Identify the blood parasite species.
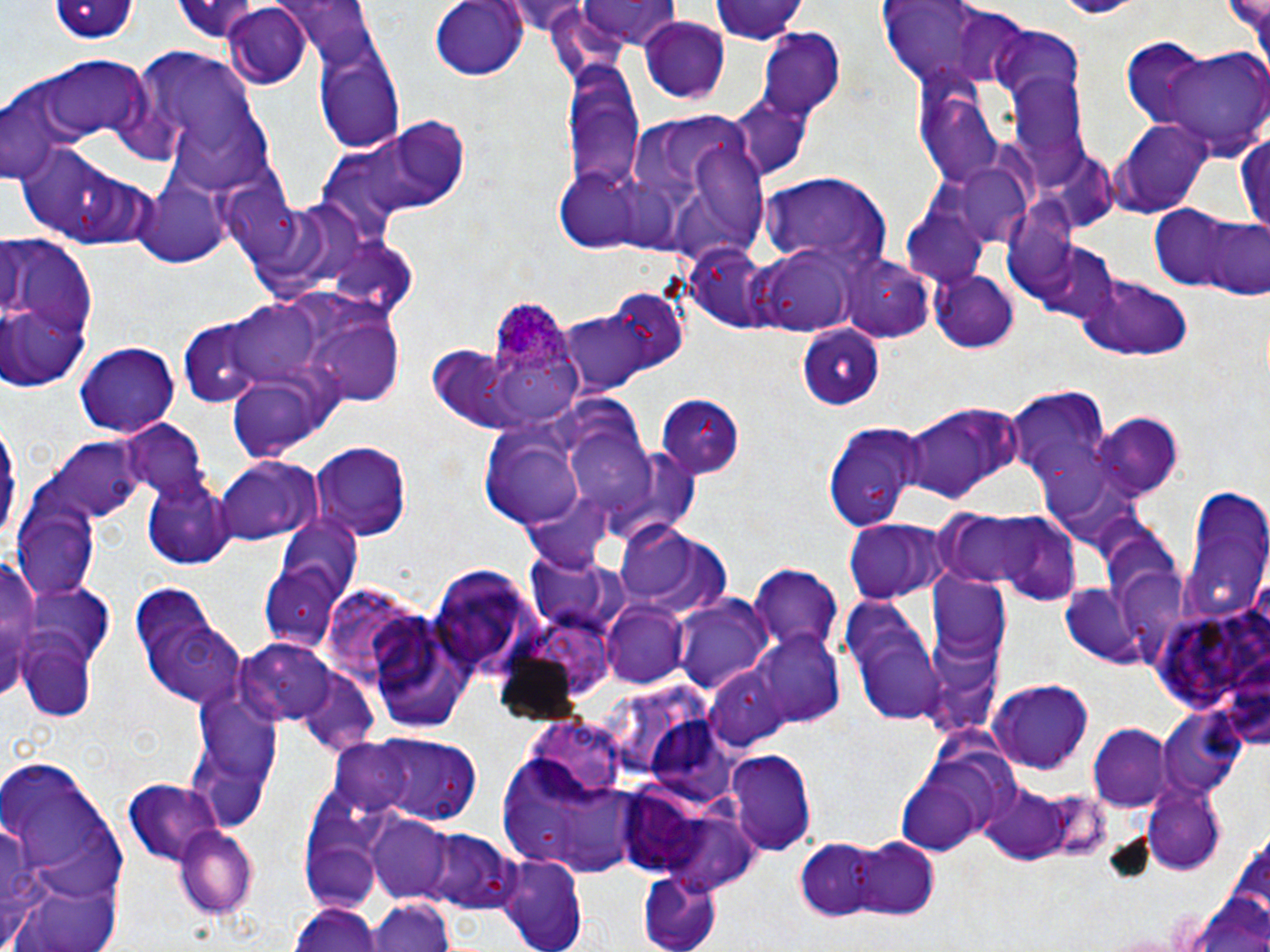

Plasmodium ovale.

{
  "magnification": "1000x",
  "image_size": "1270×952 pixels",
  "uninfected_red_blood_cell_locations": "approximate bounding boxes as (x1, y1, x2, y2) in pixels: (279, 0, 379, 73), (430, 0, 529, 82), (574, 0, 685, 50), (706, 0, 809, 44), (1231, 0, 1270, 72), (168, 1, 278, 41), (49, 2, 143, 45), (876, 3, 1021, 89), (218, 5, 312, 87), (639, 17, 731, 103), (991, 28, 1086, 113), (756, 29, 847, 120), (1136, 39, 1270, 160), (314, 45, 404, 149), (124, 46, 262, 163), (34, 55, 154, 141), (564, 57, 647, 203), (1005, 64, 1090, 179), (3, 85, 81, 186), (916, 88, 1011, 190), (729, 96, 813, 182), (174, 107, 278, 196), (623, 109, 771, 263), (315, 112, 469, 238), (1118, 120, 1215, 214), (1237, 128, 1270, 232), (23, 147, 127, 244), (948, 162, 1039, 247), (557, 167, 649, 251), (754, 171, 890, 271), (133, 176, 230, 269), (229, 182, 302, 262), (1152, 204, 1245, 292), (899, 208, 993, 288), (1186, 213, 1267, 297), (0, 226, 96, 391), (323, 235, 421, 319), (1022, 236, 1126, 326), (757, 248, 856, 334), (841, 254, 936, 342), (933, 267, 1018, 352), (1076, 274, 1195, 360), (607, 287, 691, 370), (224, 297, 331, 389), (557, 304, 664, 395), (302, 308, 405, 407), (178, 320, 262, 407), (799, 327, 885, 412), (74, 340, 181, 436), (495, 362, 600, 420), (227, 376, 331, 463), (1004, 385, 1110, 494), (654, 393, 747, 477), (901, 405, 1018, 504), (1092, 415, 1183, 500), (0, 417, 21, 551), (480, 418, 581, 530), (121, 422, 211, 506), (825, 423, 927, 532), (566, 432, 663, 518), (43, 439, 143, 525), (311, 442, 409, 539), (213, 457, 324, 546), (143, 475, 234, 569), (1179, 487, 1269, 621), (523, 492, 614, 575), (14, 508, 98, 600), (939, 509, 1083, 601), (274, 515, 362, 608), (844, 517, 946, 604), (612, 521, 732, 620), (3, 550, 38, 697), (524, 554, 623, 635), (750, 565, 840, 657), (430, 566, 536, 676), (927, 575, 1013, 661), (1056, 583, 1147, 667), (130, 585, 247, 709), (675, 594, 773, 698), (841, 596, 949, 726), (1151, 598, 1270, 719), (601, 602, 689, 688), (365, 611, 478, 732), (756, 631, 848, 727), (15, 632, 100, 724), (237, 638, 346, 726), (707, 664, 792, 754), (297, 670, 382, 755), (990, 679, 1093, 771), (184, 682, 284, 828), (1158, 711, 1246, 800), (646, 721, 741, 809), (1089, 725, 1169, 808), (339, 735, 489, 829), (493, 741, 647, 877), (2, 750, 126, 938), (726, 750, 816, 857), (897, 759, 994, 856), (123, 779, 228, 867), (1141, 780, 1226, 873), (980, 784, 1072, 861), (657, 811, 760, 897), (302, 816, 384, 909), (367, 816, 451, 904), (171, 824, 261, 919), (413, 828, 520, 912), (797, 838, 884, 920), (849, 838, 940, 920), (496, 853, 588, 952), (639, 870, 721, 952), (15, 881, 123, 952), (1186, 884, 1270, 952), (369, 896, 455, 952), (291, 902, 382, 952)",
  "plasmodium_ovale_infected_red_blood_cell_locations": "approximate bounding boxes as (x1, y1, x2, y2) in pixels: (490, 297, 569, 373)",
  "modality": "optical microscopy",
  "preparation": "thin blood film",
  "field_of_view": "single",
  "white_blood_cell_locations": "approximate bounding boxes as (x1, y1, x2, y2) in pixels: (0, 751, 130, 943)",
  "stain": "May-Grünwald-Giemsa"
}